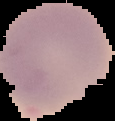

From a thin blood film. Result: no malaria parasites detected. Cell region segmented out of the field of view; the surrounding area is masked to black. Image is 115×121 pixels.